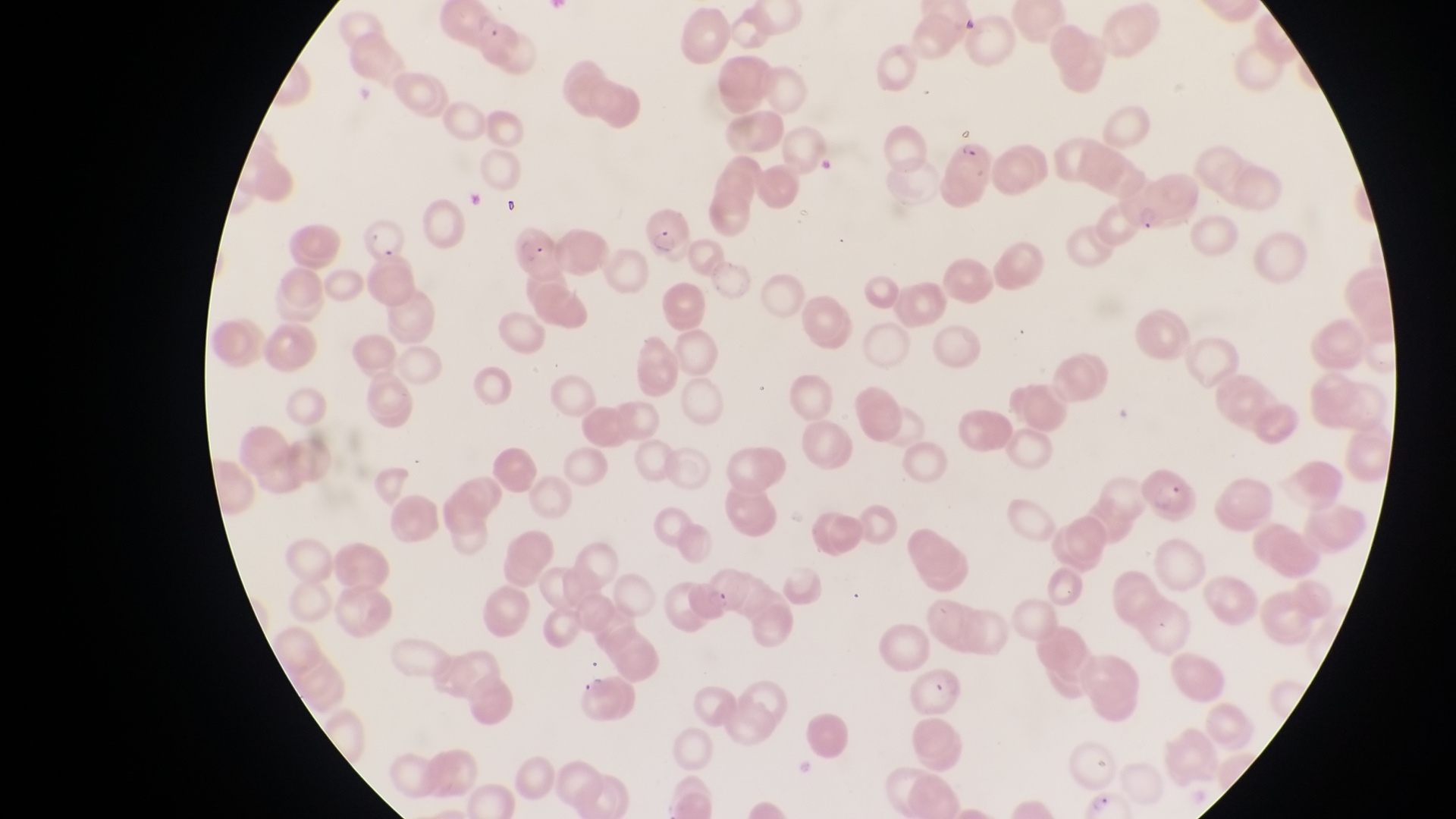

Approximate bounding boxes as {left, top, right, bottom} in pixels.
Summary:
  - Parasitised red blood cell locations: {438, 2, 514, 62}, {946, 140, 995, 192}, {1120, 168, 1173, 237}, {637, 208, 693, 264}, {362, 222, 404, 272}
  - Capture: smartphone photograph through the eyepiece of an Olympus CX-23 microscope
  - Country: Uganda
  - Field of view: single
  - Preparation: thin blood smear
  - Magnification: 1000x
  - Image size: 1456×819 pixels